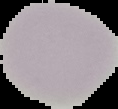

image_size: 118×109 pixels
result: no Plasmodium parasites seen
image_type: cell region segmented out of the field of view; surrounding area masked to black
preparation: thin blood film